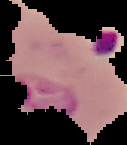

Summary:
  - Result: Plasmodium parasites detected
  - Image size: 127×145 pixels
  - Preparation: thin blood film
  - Image type: segmented cell region with the area outside set to black